Identify the parasite.
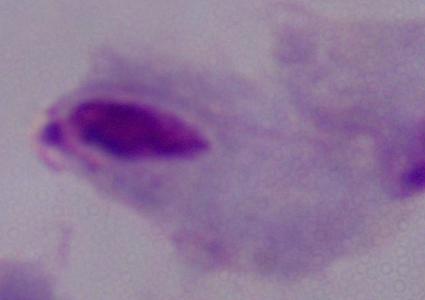

A trichomonad.

modality = micrograph
magnification = 1000x